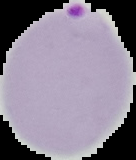
{
  "image_size": "136×160 pixels",
  "image_type": "cell region segmented out of the field of view; surrounding area masked to black",
  "preparation": "thin blood film",
  "malaria_status": "parasitized"
}